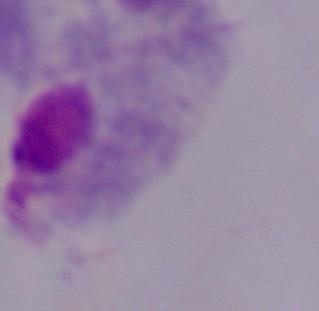

Summary:
  - Identification: trichomonad
  - Magnification: 1000x
  - Modality: photomicrograph